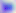 Captured at 400x magnification. Toxoplasma gondii is shown. Micrograph.